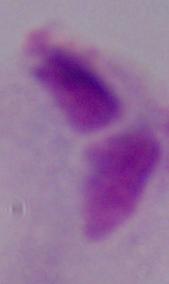

1000x magnification. A trichomonad is seen. Photomicrograph.